Classify this cell by malaria status.
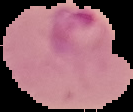
Parasitized.

Image is 133×112 pixels. Cell region segmented out of the field of view; the surrounding area is masked to black. From a thin blood film.